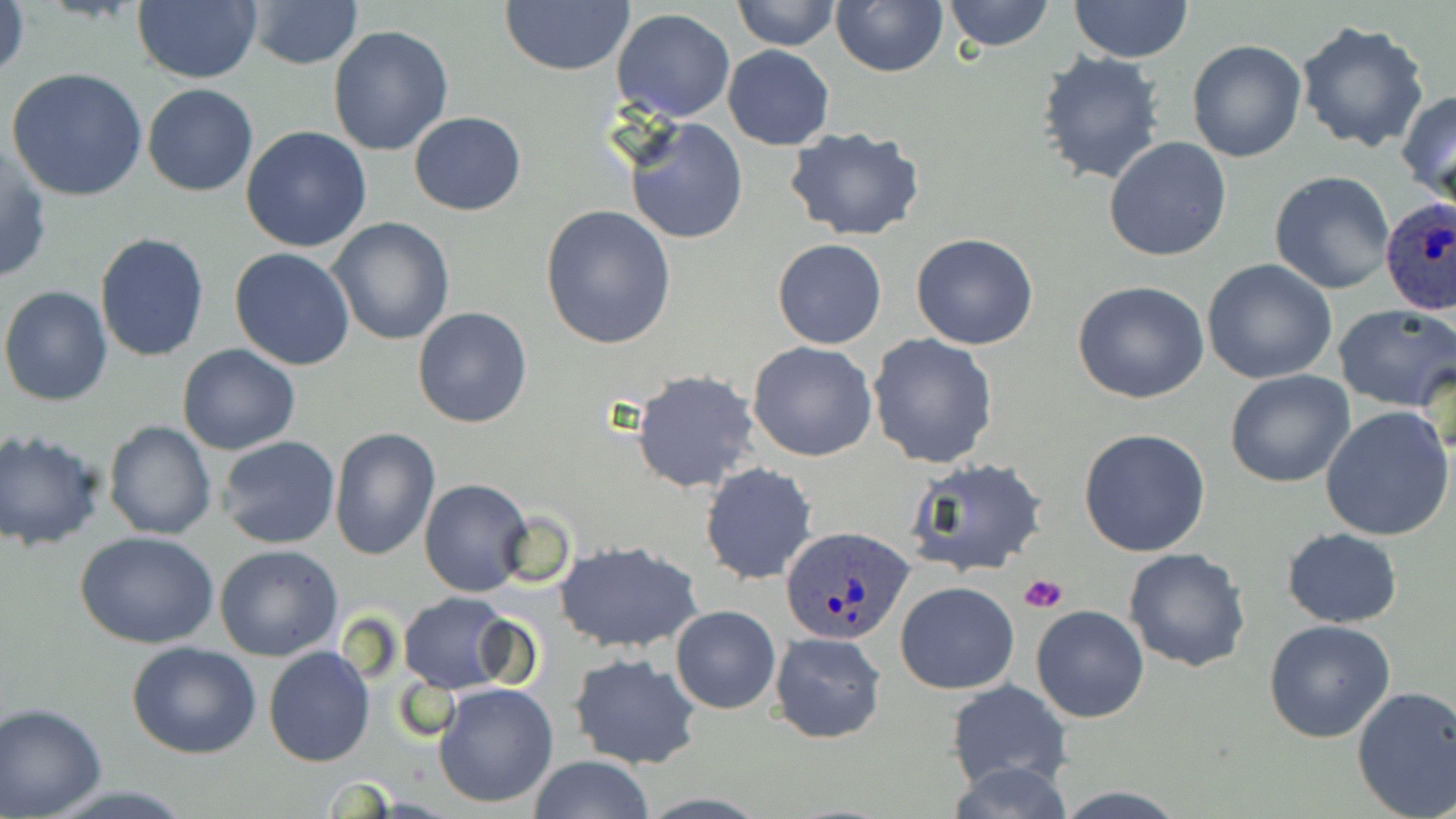
slide-level diagnosis = Plasmodium ovale
field of view = one of a larger specimen
modality = light microscopy
magnification = 1000x
platelet locations = approximate bounding boxes as (x1, y1, x2, y2) in pixels: (1019, 573, 1067, 614)
Plasmodium ovale-infected red blood cell locations = approximate bounding boxes as (x1, y1, x2, y2) in pixels: (1378, 196, 1454, 313), (781, 526, 915, 646)
uninfected red blood cell locations = approximate bounding boxes as (x1, y1, x2, y2) in pixels: (1, 0, 30, 85), (731, 0, 838, 50), (942, 0, 1055, 51), (1069, 0, 1191, 62), (245, 1, 363, 70), (831, 1, 948, 77), (132, 2, 261, 84), (500, 2, 634, 77), (612, 8, 735, 123), (1295, 20, 1429, 152), (327, 25, 453, 157), (1187, 39, 1307, 163), (721, 45, 834, 150), (1035, 50, 1167, 186), (6, 67, 149, 201), (142, 83, 258, 197), (1398, 87, 1456, 208), (409, 111, 527, 216), (622, 118, 749, 245), (240, 125, 372, 251), (784, 126, 926, 242), (1103, 137, 1232, 262), (0, 143, 51, 284), (1269, 171, 1397, 294), (539, 205, 677, 349), (328, 218, 455, 345), (95, 232, 211, 360), (910, 232, 1039, 350), (772, 238, 887, 349), (228, 247, 356, 370), (1203, 259, 1337, 385), (1072, 281, 1210, 404), (1, 284, 115, 406), (1332, 304, 1456, 413), (411, 307, 533, 429), (868, 332, 999, 468), (747, 341, 877, 462), (178, 343, 302, 456), (1225, 369, 1356, 488), (631, 370, 760, 494), (1321, 406, 1455, 542), (103, 421, 215, 540), (329, 427, 442, 560), (0, 428, 106, 549), (1079, 428, 1210, 557), (218, 436, 341, 550), (902, 456, 1050, 579), (700, 463, 819, 585), (418, 477, 533, 596), (1280, 528, 1403, 627), (75, 529, 219, 649), (555, 539, 703, 654), (214, 545, 344, 661), (1123, 547, 1252, 673), (894, 581, 1018, 694), (398, 592, 517, 693), (669, 605, 780, 714), (1031, 605, 1149, 723), (1264, 618, 1396, 743), (769, 631, 888, 742), (127, 640, 261, 759), (263, 646, 376, 767), (570, 652, 702, 770), (432, 680, 560, 809), (946, 680, 1073, 792), (1352, 685, 1456, 819), (0, 704, 109, 818), (527, 755, 656, 819), (944, 762, 1073, 819)
stain = May-Grünwald-Giemsa
preparation = thin blood smear
image size = 1456×819 pixels